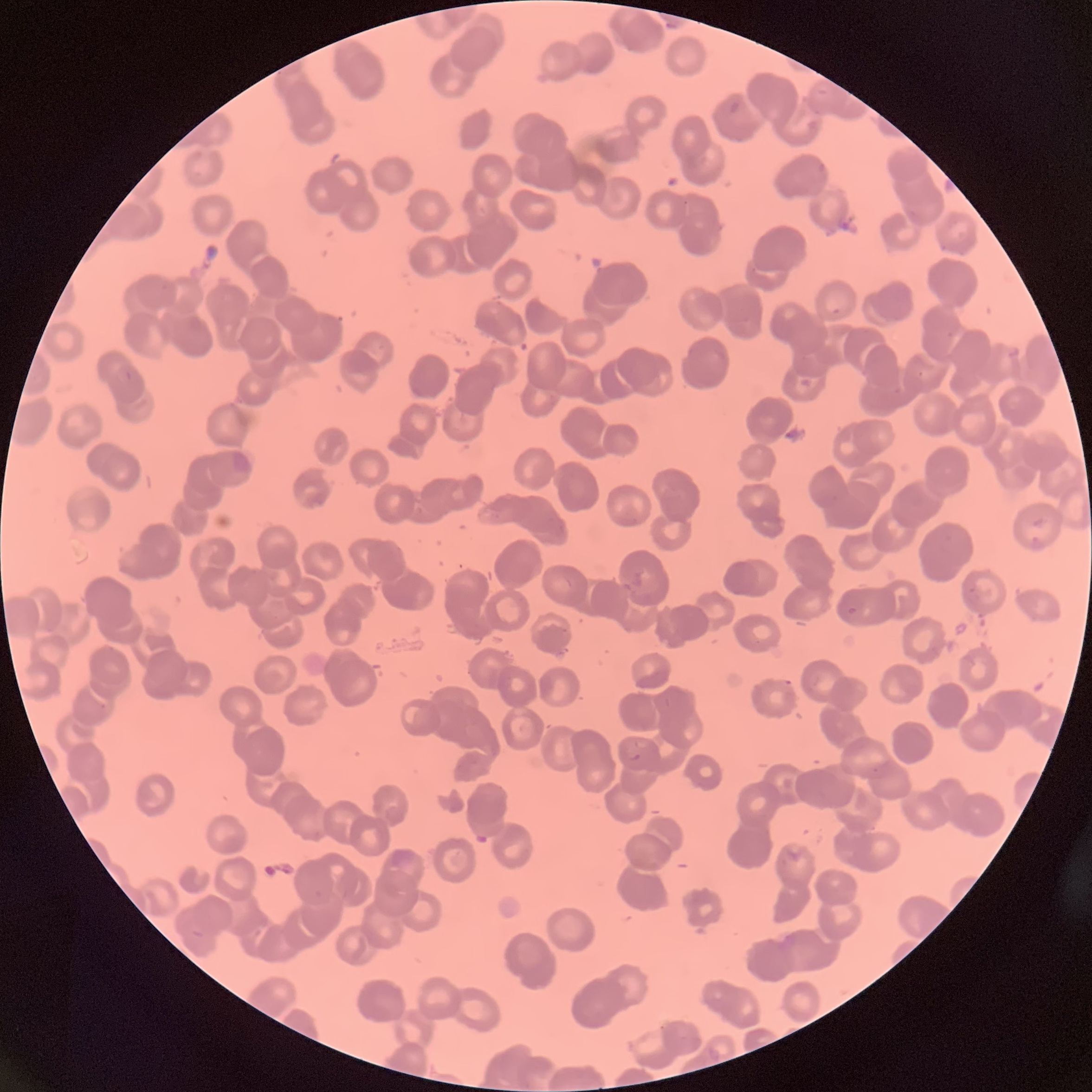
coordinate format = approximate bounding boxes as (x1, y1, x2, y2) in pixels
Plasmodium parasite locations = (729, 100, 740, 114), (826, 304, 842, 314), (784, 679, 794, 688), (627, 748, 640, 761)
modality = optical microscopy
red blood cell morphology = rouleaux formation
preparation = thin blood smear
image size = 1092×1092 pixels